Report the malaria status of this cell.
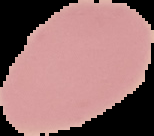

It is uninfected.

image type = segmented cell region with the area outside set to black
preparation = thin blood film
image size = 154×136 pixels